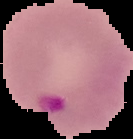

image size = 133×139 pixels
result = Plasmodium parasites detected
image type = cell region segmented out of the field of view; surrounding area masked to black
preparation = thin blood smear